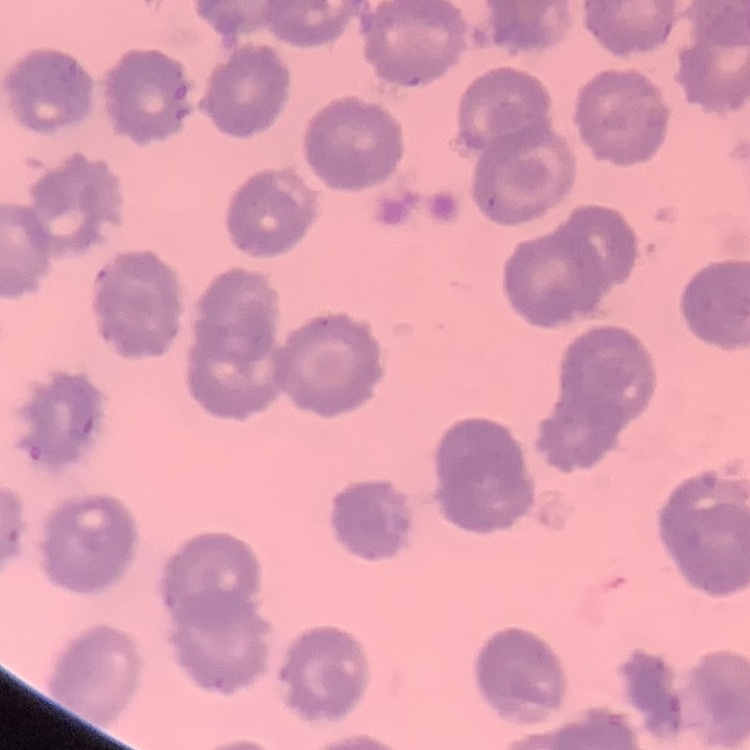

Summary:
  - Erythrocyte morphology: no rouleaux formation
  - Image type: square crop of a larger photomicrograph
  - Stain: Field's or Giemsa
  - Preparation: thin peripheral smear